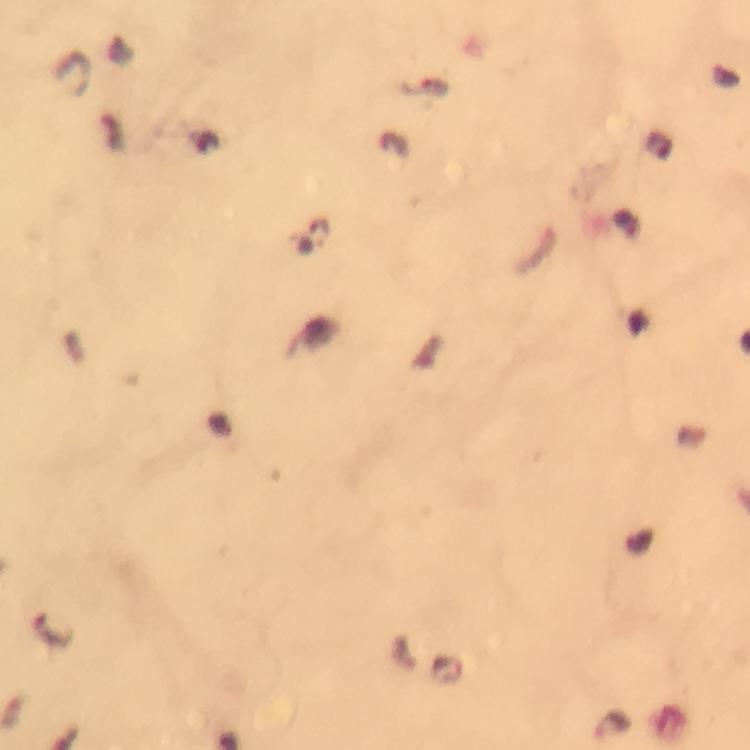
magnification: 100x
preparation: thick blood film
capture: smartphone mounted on the microscope
cropped_from: a single field of view
context: from a diagnostic examination for malaria
plasmodium_parasite_locations: 'approximate object centers, in pixels from the top-left corner: (x=612, y=724)'
stain: Giemsa
image_size: 750×750 pixels
immersion_oil: used